Assess this cell for malaria.
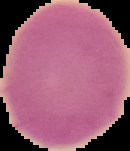
It is uninfected.

image size = 130×151 pixels
image type = segmented cell region with the area outside set to black
preparation = thin blood smear